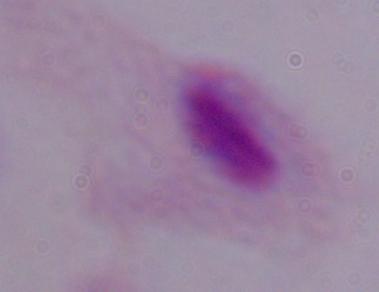

Summary:
  - Magnification: 1000x
  - Modality: micrograph
  - Identification: trichomonad